Report the malaria status of this cell.
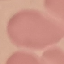

It is uninfected.

Thin blood film. Acquired by smartphone through the microscope eyepiece. Automatically extracted cell patch, resized to 64 × 64 pixels. Giemsa-stained preparation.